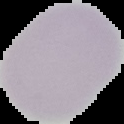
Summary:
  - Malaria status: uninfected
  - Preparation: thin blood smear
  - Image type: segmented cell region with the area outside set to black
  - Image size: 124×124 pixels